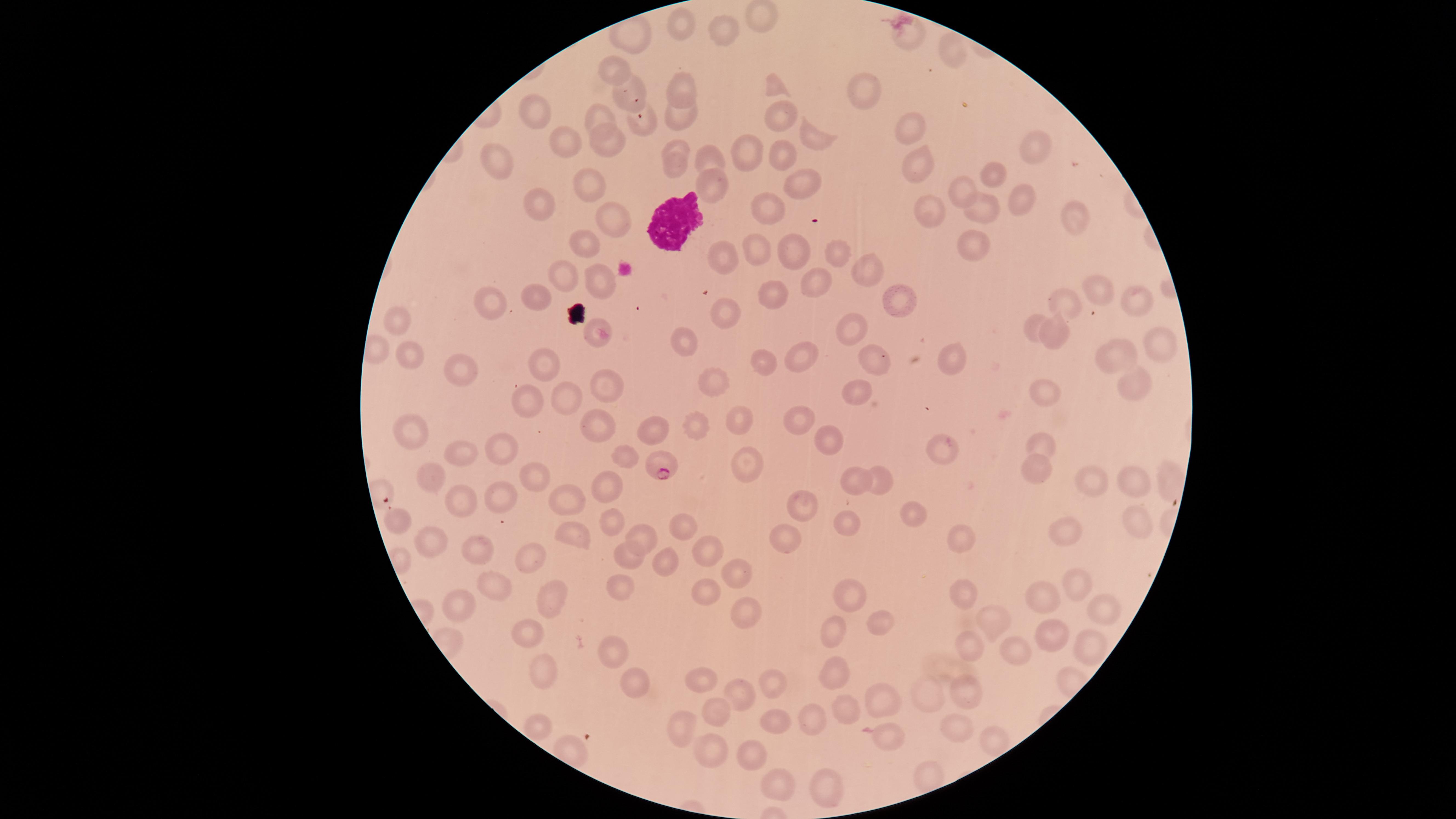 Approximate marker points as [x, y] in pixels. WBCs: [673, 226]. Uninfected RBCs: [759, 16], [679, 25], [724, 29], [906, 37], [951, 53], [617, 72], [776, 86], [683, 89], [629, 92], [866, 92], [776, 113], [534, 114], [596, 119], [680, 119], [644, 123], [911, 126], [813, 138], [565, 140], [613, 142], [1029, 148], [676, 150], [745, 154], [777, 154], [708, 157], [923, 161], [500, 164], [673, 170], [990, 173], [590, 184], [800, 184], [709, 187], [958, 191], [1022, 201], [550, 204], [767, 207], [928, 212], [977, 213], [613, 218], [1073, 222], [973, 245], [584, 247], [762, 247], [827, 251], [795, 256], [716, 262], [869, 265], [564, 273], [599, 278], [812, 284], [1097, 294], [764, 295], [537, 296], [1135, 298], [487, 302], [894, 302], [1068, 303], [724, 315], [1032, 325], [394, 326], [593, 326], [1057, 328], [855, 329], [1163, 343], [683, 347], [804, 355], [1115, 355], [413, 356], [950, 357], [875, 358], [762, 361], [540, 368], [457, 369], [713, 380], [1131, 382], [603, 383], [859, 392], [1050, 393], [560, 401], [526, 403], [736, 414], [798, 414], [695, 423], [598, 432], [656, 432], [415, 435], [831, 437], [1043, 441], [502, 447], [940, 447], [462, 452], [626, 455], [744, 466], [1035, 466], [533, 474], [435, 475], [854, 477], [1087, 480], [1136, 480], [877, 483], [608, 487], [499, 499], [566, 499], [807, 499], [455, 501], [912, 513], [397, 520], [615, 521], [681, 524], [1137, 524], [846, 525], [1068, 530], [789, 535], [957, 536], [571, 537], [430, 540], [638, 540], [708, 548], [472, 551], [629, 555], [534, 557], [662, 557], [736, 570], [493, 582], [620, 585], [1077, 586], [960, 590], [707, 594], [1044, 595], [848, 596], [554, 600], [455, 607], [744, 611], [1101, 615], [881, 621], [994, 621], [1055, 630], [836, 632], [528, 633], [1085, 643], [973, 646], [611, 648], [1018, 653], [545, 668], [634, 677], [835, 677], [706, 681], [773, 683], [736, 691], [934, 692], [964, 694], [881, 695], [719, 710], [845, 712], [774, 717], [809, 723], [536, 726], [690, 727], [958, 728], [884, 732], [990, 735], [708, 743], [756, 754], [777, 778], [824, 785]. Parasitized RBCs: [658, 466]. Smartphone photograph through the microscope eyepiece. Single field of view. Giemsa stain. Thin blood film. Image is 1456×819 pixels. Species: Plasmodium falciparum. The visible region is circular. Presence: malaria parasites identified.